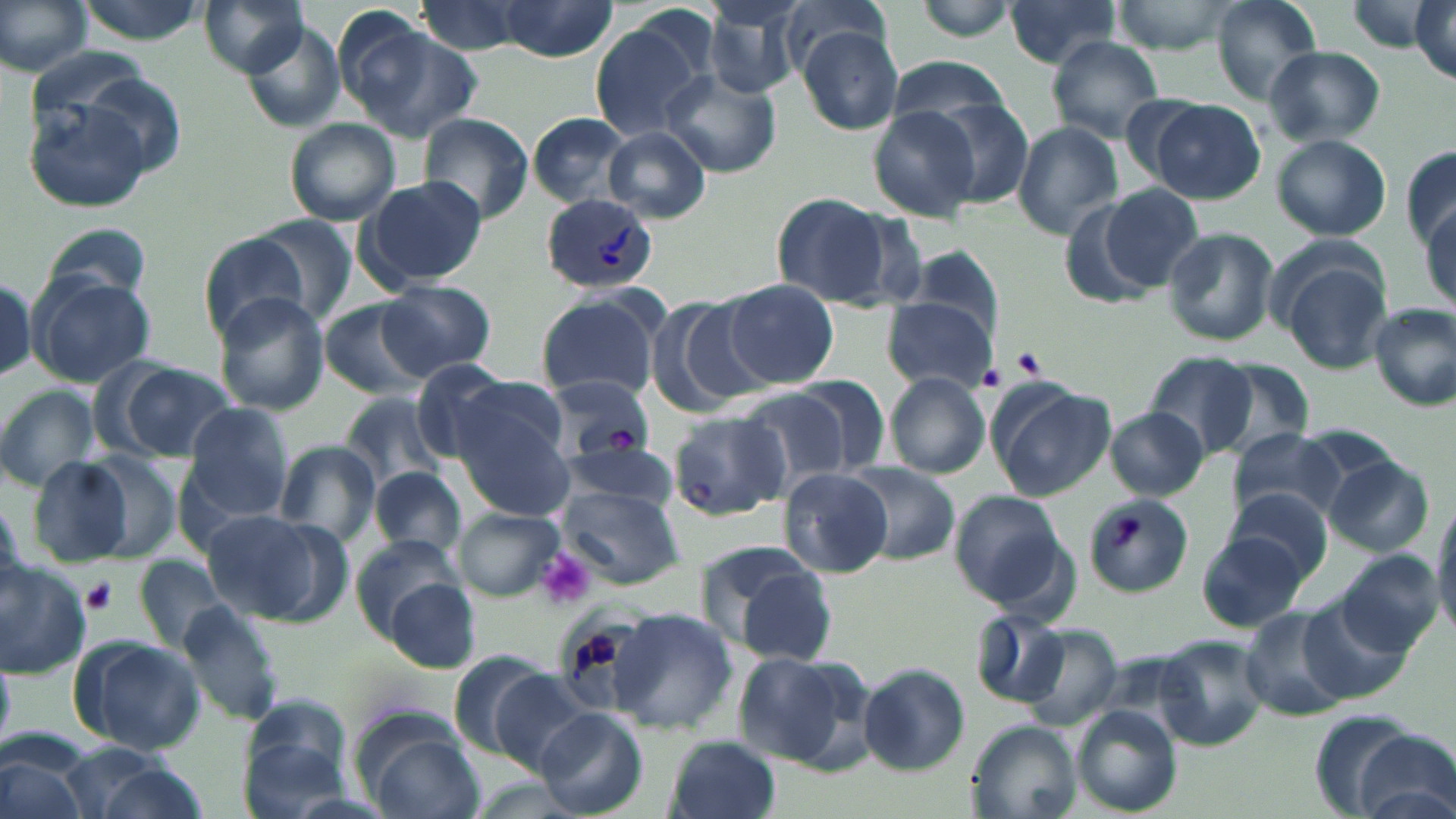
Approximate bounding boxes as (x1,y1)-(x2,y2) corner pairs in pixels. Platelet locations: (1010,347)-(1047,379), (978,365)-(1008,392), (1108,516)-(1142,550), (533,548)-(595,612), (80,578)-(119,615). Plasmodium vivax-infected red blood cell locations: (541,194)-(659,293). Uninfected red blood cell locations: (0,0)-(92,78), (199,0)-(309,76), (414,0)-(533,58), (495,0)-(618,60), (778,0)-(888,77), (914,0)-(1019,40), (1000,0)-(1127,70), (1108,0)-(1243,54), (1210,0)-(1323,102), (1412,1)-(1455,81), (703,2)-(805,99), (588,16)-(712,139), (238,21)-(349,131), (349,25)-(482,142), (797,27)-(903,136), (1044,37)-(1166,142), (1263,45)-(1386,146), (885,57)-(1015,131), (661,69)-(780,177), (22,96)-(161,215), (918,97)-(1034,206), (1148,98)-(1266,204), (868,105)-(982,220), (418,112)-(534,223), (527,113)-(629,207), (284,119)-(401,226), (1013,122)-(1125,239), (604,127)-(712,221), (1271,134)-(1391,240), (1401,145)-(1456,255), (361,176)-(487,289), (1099,185)-(1204,292), (772,192)-(892,306), (1114,195)-(1264,318), (1056,198)-(1158,307), (1421,207)-(1455,310), (252,217)-(357,324), (43,224)-(154,306), (1161,226)-(1278,347), (201,232)-(313,339), (1284,261)-(1394,374), (30,274)-(155,387), (378,280)-(496,378), (723,281)-(840,387), (212,293)-(331,414), (536,293)-(662,401), (650,297)-(773,412), (320,298)-(433,399), (882,298)-(997,393), (1370,304)-(1456,410), (1146,352)-(1258,455), (1207,357)-(1317,455), (111,361)-(235,460), (410,361)-(516,463), (885,371)-(991,480), (785,375)-(890,478), (463,378)-(570,461), (986,378)-(1113,500), (550,379)-(656,460), (0,384)-(103,491), (734,387)-(852,490), (344,392)-(446,490), (451,402)-(574,521), (182,403)-(293,520), (1104,409)-(1210,499), (668,410)-(792,521), (1228,428)-(1345,526), (275,442)-(381,546), (561,443)-(682,511), (78,452)-(182,563), (26,454)-(146,569), (1324,456)-(1434,556), (840,461)-(960,564), (373,468)-(466,559), (778,468)-(893,576), (560,485)-(685,584), (949,489)-(1067,608), (1225,490)-(1336,586), (1082,492)-(1194,596), (1432,500)-(1456,635), (200,509)-(348,627), (455,509)-(564,600), (1197,531)-(1312,631), (352,534)-(459,633), (1336,549)-(1444,658), (723,553)-(839,664), (134,556)-(228,654), (0,559)-(90,676), (388,578)-(480,672), (1299,599)-(1413,706), (176,600)-(285,727), (608,607)-(737,732), (1239,609)-(1352,721), (972,612)-(1071,710), (1019,626)-(1122,728), (68,634)-(205,754), (1154,636)-(1271,751), (732,650)-(871,773), (858,663)-(969,775), (488,671)-(597,774), (241,699)-(353,812), (1070,708)-(1181,816), (535,709)-(648,817), (1307,711)-(1429,818), (966,720)-(1082,819), (363,721)-(482,819), (666,735)-(784,819), (1354,743)-(1456,819), (1,750)-(89,819), (92,764)-(212,819). Slide-level diagnosis: Plasmodium vivax. Thin blood film. Optical microscopy. May-Grünwald-Giemsa stain. Single field of view. 1000x magnification. Image is 1456×819 pixels.